Identify the preparation type.
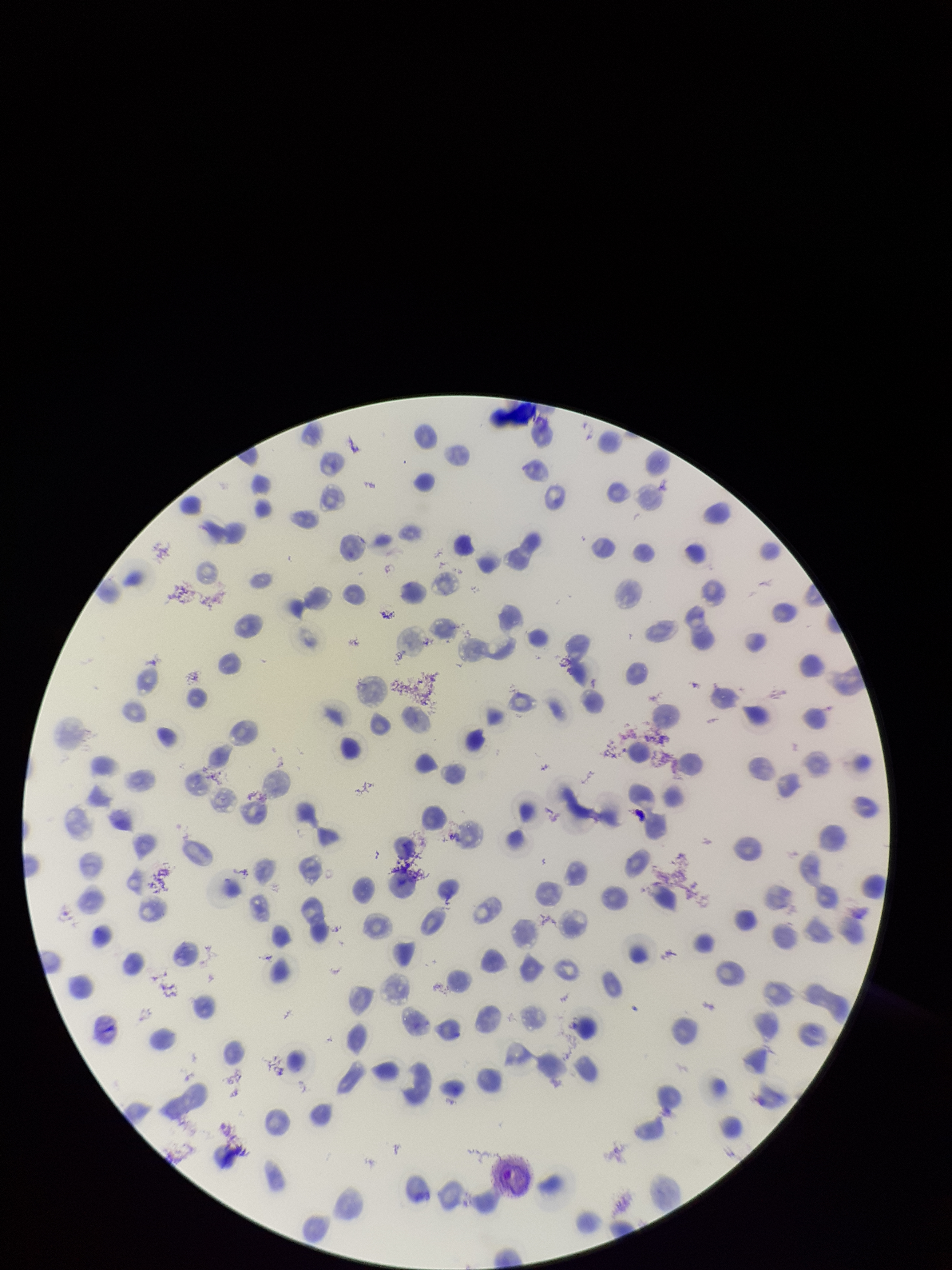
It is a thin blood smear.

Patient malaria status: infected. Red blood cell count: 156. Species reported for this patient: Plasmodium vivax. Parasitized red blood cell count: 0. Stained with Giemsa. One field from this slide. Parasitized red blood cells: none seen. Smartphone photograph taken through the eyepiece of a microscope. Image is 952×1270 pixels.